Assess this cell for malaria.
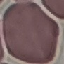
It is uninfected.

Summary:
  - Capture: smartphone through the microscope eyepiece
  - Image type: automatically extracted cell patch, resized to 64 × 64 pixels
  - Preparation: thin blood film
  - Stain: Giemsa